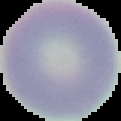
preparation = thin blood film
image size = 121×121 pixels
malaria status = uninfected
image type = segmented cell region on a black background